State which parasite is depicted.
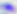
This is Toxoplasma gondii.

Summary:
  - Magnification: 400x
  - Modality: micrograph